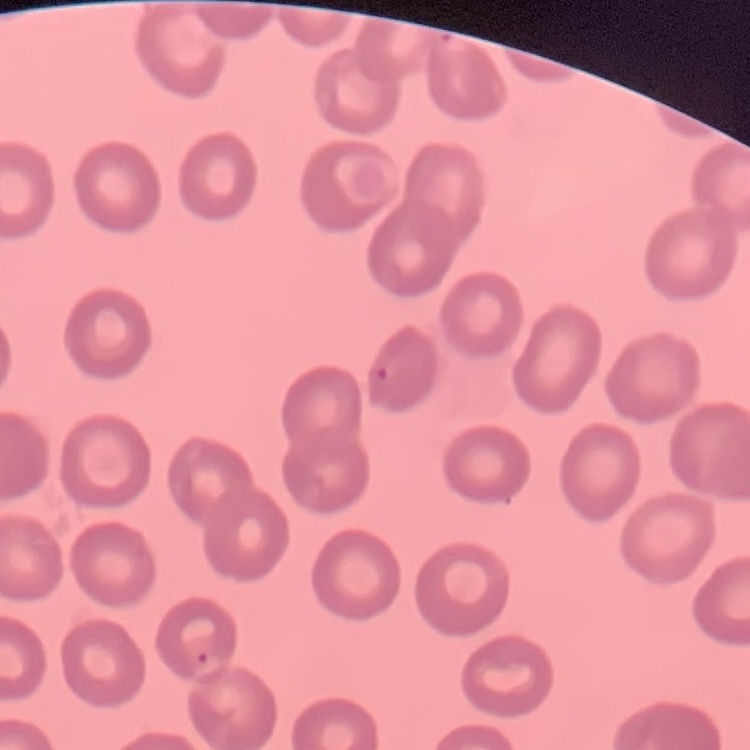
Summary:
  - Red blood cell morphology: no rouleaux formation
  - Stain: Field's or Giemsa
  - Preparation: thin blood smear
  - Image type: one tile cut from a larger photomicrograph